Give the extent of all Plasmodium ovale-infected red blood cells.
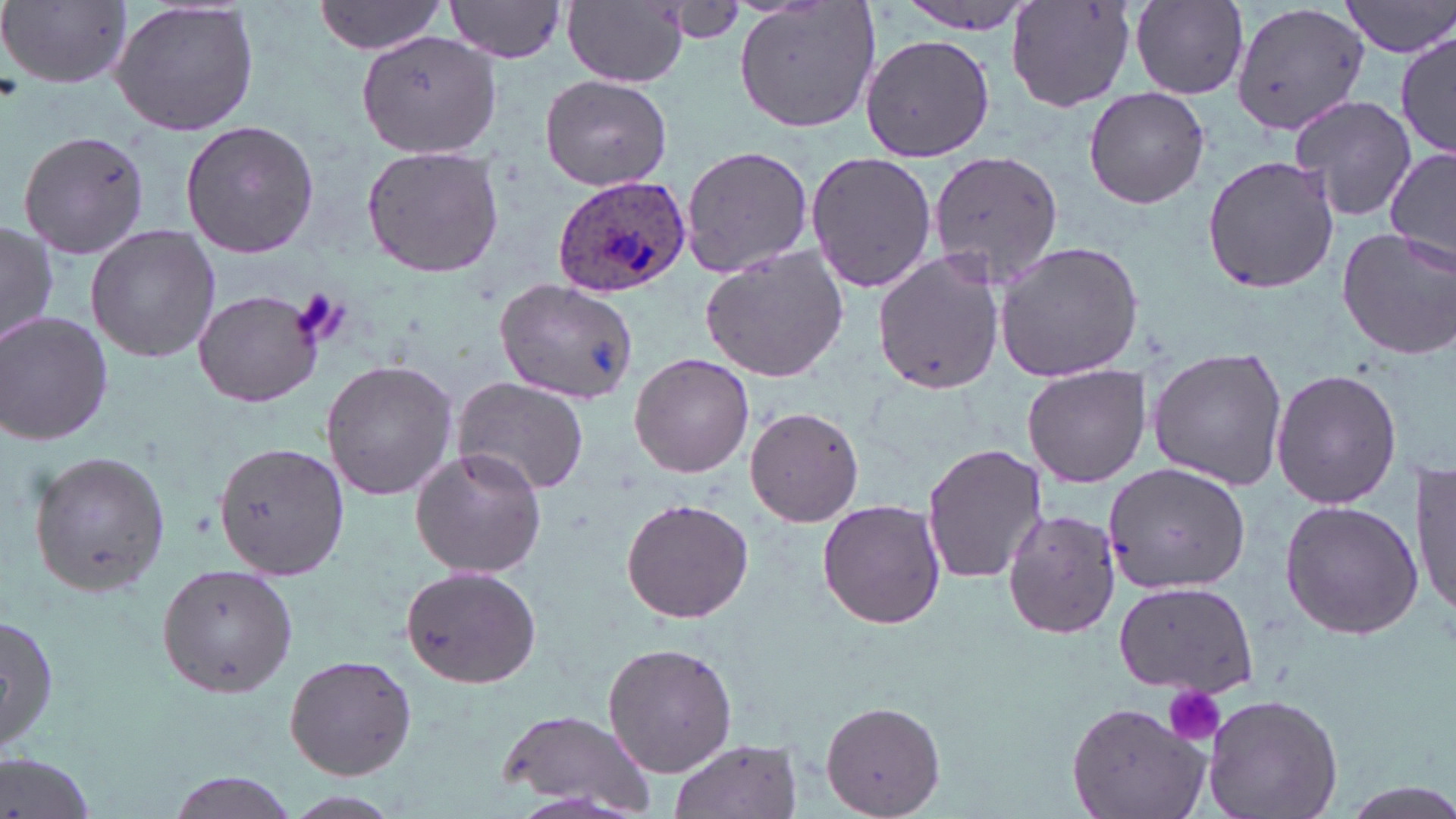
Approximate bounding boxes as [x1, y1, x2, y2] in pixels.
Plasmodium ovale-infected red blood cells: [553, 176, 692, 296].

Uninfected red blood cell locations: [1006, 0, 1139, 115], [1229, 0, 1368, 138], [1343, 0, 1454, 58], [108, 1, 262, 138], [445, 1, 570, 64], [563, 1, 687, 86], [732, 1, 883, 133], [1132, 1, 1248, 98], [3, 2, 131, 89], [314, 2, 449, 55], [894, 3, 1039, 39], [1395, 29, 1453, 159], [357, 30, 500, 159], [860, 31, 994, 164], [539, 73, 673, 193], [1083, 86, 1211, 209], [1289, 95, 1418, 220], [179, 120, 320, 258], [18, 131, 153, 259], [680, 143, 814, 280], [359, 146, 505, 280], [928, 148, 1064, 286], [1385, 148, 1456, 274], [804, 152, 938, 294], [1201, 155, 1339, 293], [1, 221, 59, 351], [85, 225, 222, 363], [1337, 227, 1456, 358], [993, 241, 1144, 381], [699, 244, 849, 381], [872, 249, 1004, 396], [495, 279, 636, 405], [193, 288, 323, 408], [0, 310, 116, 446], [1146, 349, 1288, 489], [629, 354, 754, 477], [321, 359, 458, 502], [1019, 364, 1152, 486], [1272, 368, 1403, 510], [452, 375, 590, 497], [745, 406, 865, 527], [214, 441, 348, 581], [921, 442, 1046, 587], [409, 448, 548, 579], [27, 452, 172, 596], [1414, 458, 1455, 619], [1103, 463, 1249, 594], [620, 497, 754, 623], [816, 498, 947, 630], [1279, 500, 1422, 640], [1001, 506, 1124, 643], [156, 563, 299, 698], [399, 567, 543, 689], [1113, 578, 1258, 695], [2, 613, 58, 754], [602, 640, 737, 777], [283, 655, 418, 782], [1200, 693, 1345, 819], [818, 699, 949, 819], [1067, 701, 1212, 819], [494, 707, 664, 817], [666, 738, 803, 819], [0, 752, 99, 819], [162, 770, 301, 819], [280, 791, 405, 819]. Platelet locations: [291, 287, 348, 346], [1163, 684, 1226, 748]. Slide-level diagnosis: Plasmodium ovale. Single field of view. May-Grünwald-Giemsa-stained preparation. 1000x magnification. Light microscopy. Image is 1456×819 pixels. Thin blood smear.